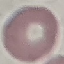
Summary:
  - Malaria status: uninfected
  - Stain: Giemsa
  - Image type: automatically extracted cell patch, resized to 64 × 64 pixels
  - Capture: smartphone through the microscope eyepiece
  - Preparation: thin blood film